Give the position of every leukocyte visible.
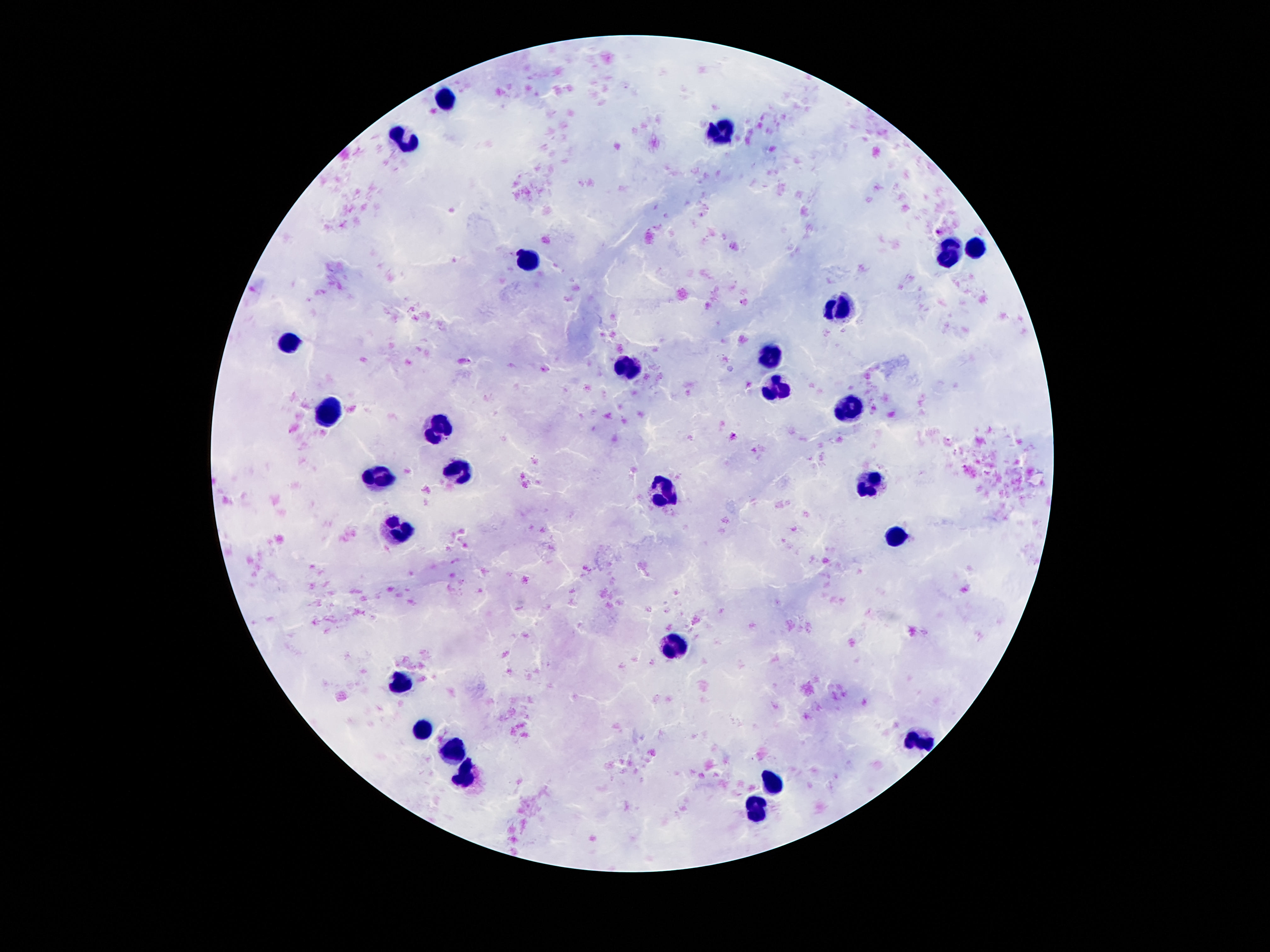

Approximate centers as (x, y) in pixels.
Leukocytes: (443, 99), (721, 132), (404, 143), (975, 247), (949, 251), (531, 260), (844, 306), (290, 343), (772, 354), (628, 370), (772, 386), (331, 411), (849, 412), (438, 427), (456, 471), (381, 479), (871, 479), (663, 493), (401, 530), (894, 534), (676, 645), (399, 684), (424, 732), (923, 745), (456, 749), (468, 777), (774, 783), (755, 810).

capture = smartphone camera through the microscope eyepiece
magnification = 100x
patient malaria status = negative
image size = 1270×952 pixels
stain = Giemsa
field of view = one from this slide
preparation = thick blood film